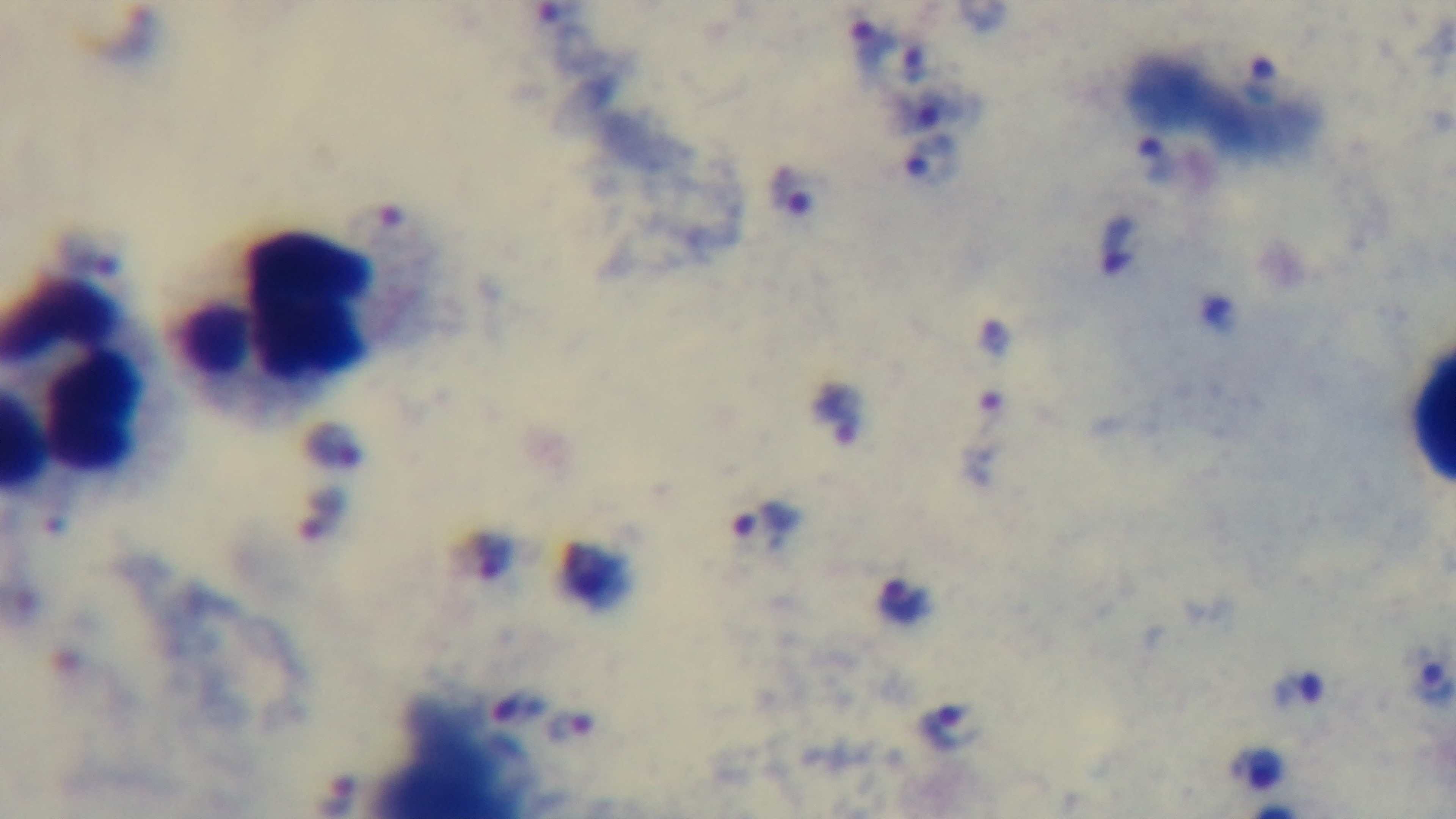

Summary:
  - Capture: mounted 4K digital camera
  - Stain: Giemsa
  - Objective: 100x oil immersion
  - Preparation: thick blood film
  - Modality: light microscopy
  - Malaria status: infected
  - Field of view: one from the slide